Locate every blood parasite and identify its species.
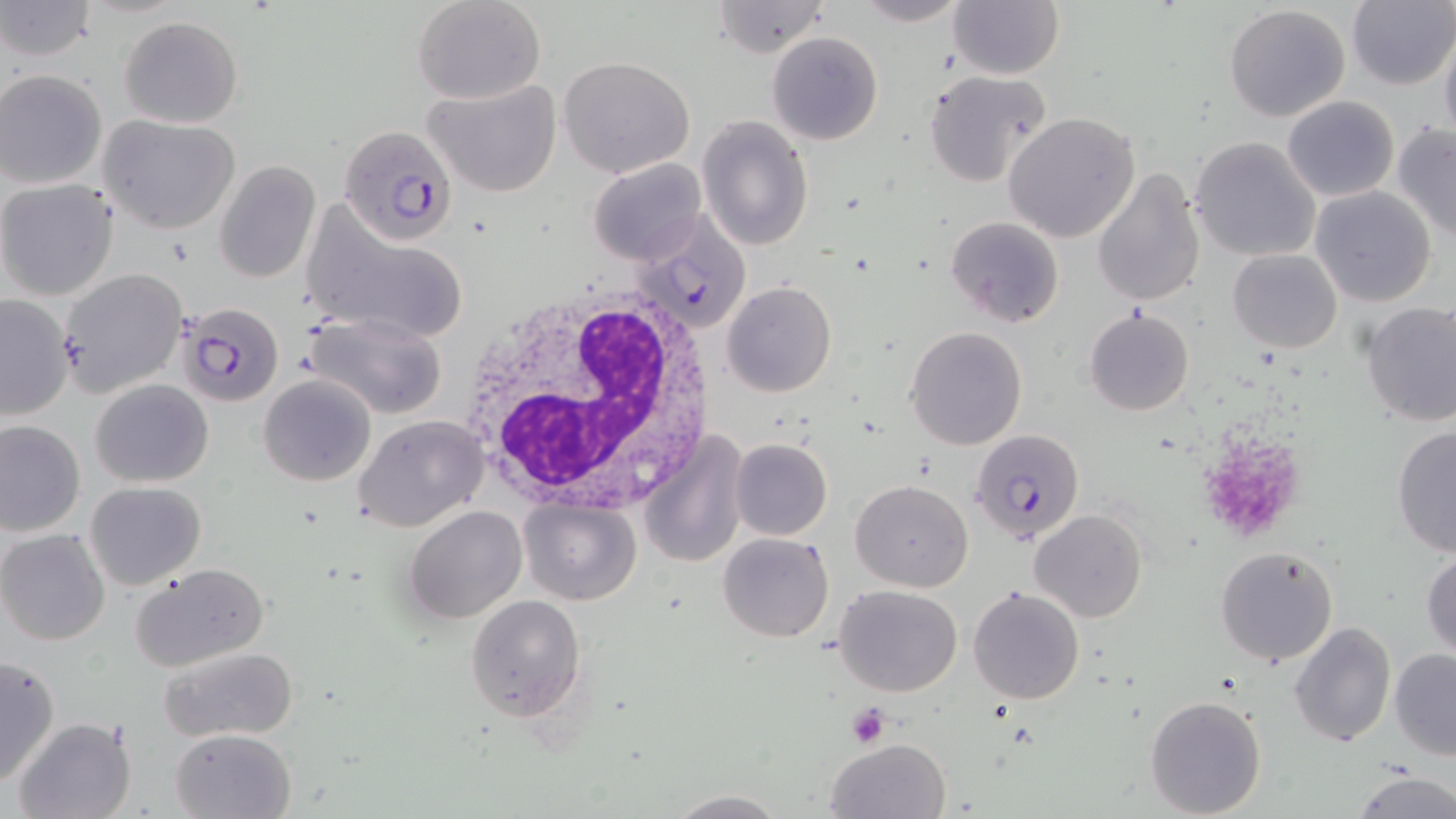

Approximate bounding boxes as (x1,y1)-(x2,y2) corner pairs in pixels.
Plasmodium falciparum-infected red blood cells: (338,122)-(461,247), (629,212)-(764,330), (173,300)-(284,404), (970,427)-(1086,546).
No Plasmodium ovale, Plasmodium malariae, Plasmodium vivax, Babesia divergens, or Trypanosoma brucei observed.

Platelet locations: (1201,437)-(1308,538), (845,702)-(892,747). White blood cell locations: (451,288)-(723,514). Uninfected red blood cell locations: (412,0)-(547,104), (854,0)-(971,26), (1,1)-(97,62), (710,1)-(833,57), (948,1)-(1063,78), (1345,1)-(1456,90), (1223,4)-(1351,121), (119,16)-(242,127), (1439,29)-(1456,151), (768,32)-(883,145), (558,54)-(697,177), (1,68)-(109,189), (922,69)-(1052,187), (422,77)-(562,197), (1282,95)-(1398,202), (1004,112)-(1140,244), (697,115)-(814,251), (98,116)-(241,234), (1392,123)-(1456,242), (1189,135)-(1322,262), (588,158)-(707,267), (214,161)-(321,283), (1092,167)-(1207,307), (0,180)-(118,300), (1309,186)-(1437,308), (299,206)-(473,349), (945,216)-(1064,328), (1227,249)-(1342,352), (57,268)-(188,399), (721,281)-(836,397), (0,294)-(74,422), (1360,302)-(1456,428), (1084,307)-(1195,416), (305,311)-(450,419), (904,326)-(1028,450), (259,373)-(377,488), (91,378)-(215,487), (355,416)-(487,531), (0,419)-(85,536), (1392,424)-(1456,557), (640,434)-(744,570), (730,437)-(832,541), (850,479)-(973,591), (84,481)-(206,589), (518,498)-(640,604), (404,506)-(526,624), (1029,509)-(1147,624), (0,529)-(111,646), (717,533)-(834,642), (1215,545)-(1339,666), (1421,549)-(1455,661), (131,563)-(270,673), (834,584)-(962,697), (969,586)-(1084,704), (465,594)-(587,722), (1289,621)-(1395,748), (160,646)-(298,743), (1388,648)-(1456,762), (0,653)-(61,787), (1145,695)-(1266,817), (13,716)-(138,819), (171,728)-(295,818), (825,738)-(950,819), (1350,772)-(1455,819), (665,791)-(790,818). Slide-level diagnosis: Plasmodium falciparum. Single field of view. Captured at 1000x magnification. Light microscopy. Thin blood film. May-Grünwald-Giemsa stain. Image is 1456×819 pixels.